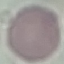 Result: no malaria parasites seen. Acquired by smartphone through the microscope eyepiece. Automatically extracted cell patch, resized to 64 × 64 pixels. Thin blood smear. Giemsa-stained preparation.